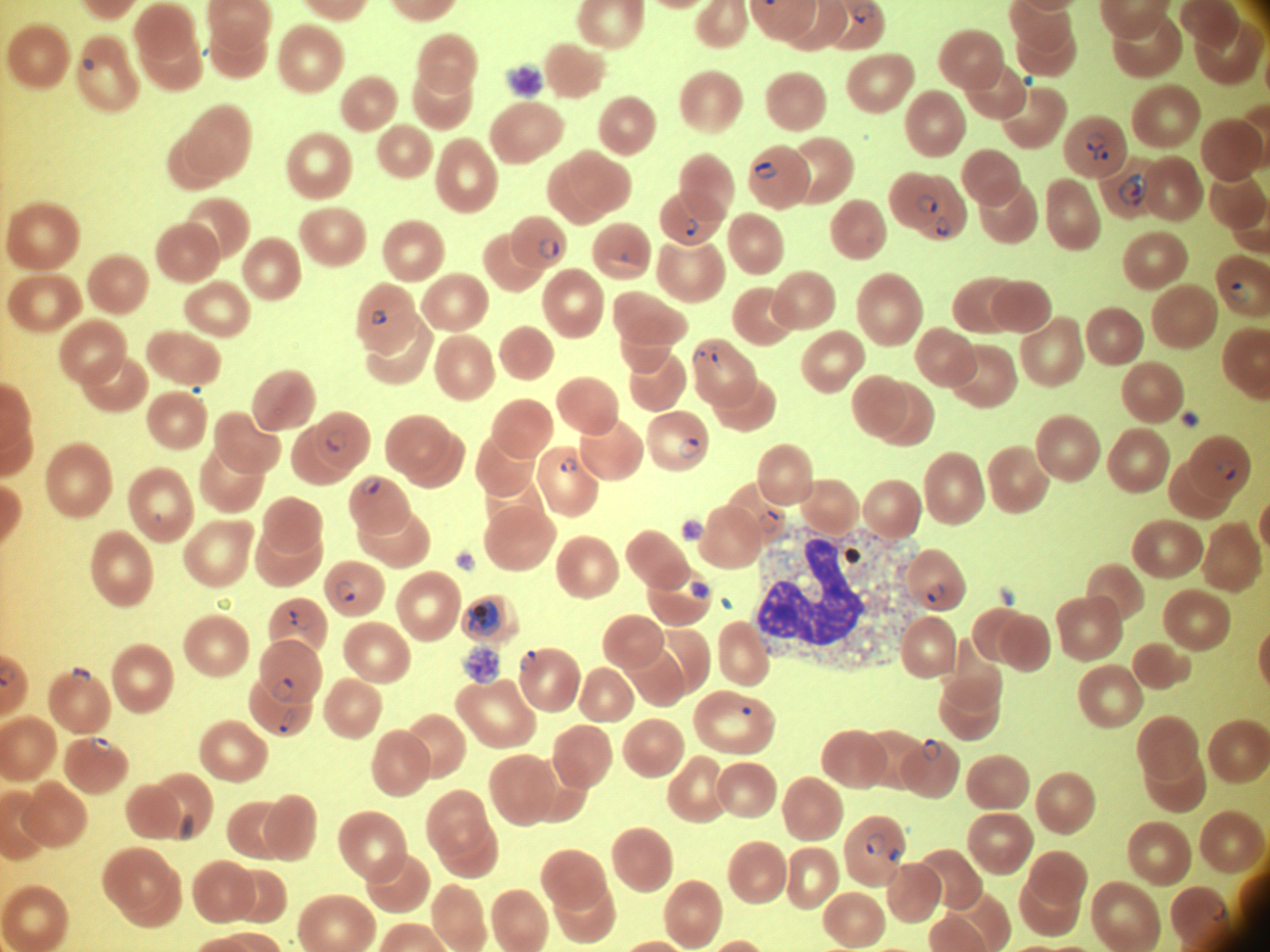
Approximate bounding boxes as (x1, y1, x2, y2) in pixels, from the source annotation, which is not necessarily exhaustive.
Summary:
  - Trophozoite locations: (468, 599, 501, 636)
  - Ring form locations: (852, 1, 875, 23), (1086, 132, 1106, 162), (1101, 151, 1109, 160), (754, 162, 777, 179), (1118, 173, 1149, 206), (916, 196, 937, 214), (936, 216, 951, 237), (683, 217, 700, 235), (539, 238, 560, 259), (1229, 282, 1249, 304), (371, 310, 389, 325), (326, 429, 347, 452), (679, 438, 701, 459), (560, 458, 578, 473), (1218, 459, 1238, 479), (361, 477, 381, 494), (759, 511, 779, 533), (336, 580, 357, 602), (927, 583, 944, 603), (289, 611, 314, 629), (520, 650, 539, 671), (71, 666, 91, 683), (271, 678, 294, 702), (280, 709, 294, 732), (90, 736, 111, 755), (922, 738, 941, 761), (866, 834, 886, 855), (888, 848, 904, 866), (1207, 901, 1225, 921)
  - Life-cycle stages among the annotated parasites: ring form, trophozoite
  - Species: Plasmodium falciparum
  - Preparation: thin blood film
  - Microscope: Leica DM2000 with built-in camera
  - Stain: Giemsa
  - Magnification: 100x
  - Field of view: single
  - Image size: 1270×952 pixels